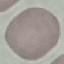

malaria_status: uninfected
preparation: thin smear
stain: Giemsa
capture: smartphone camera at the microscope eyepiece
image_type: cell patch, automatically extracted from a larger field of view and resized to 64 × 64 pixels